Outline platelets.
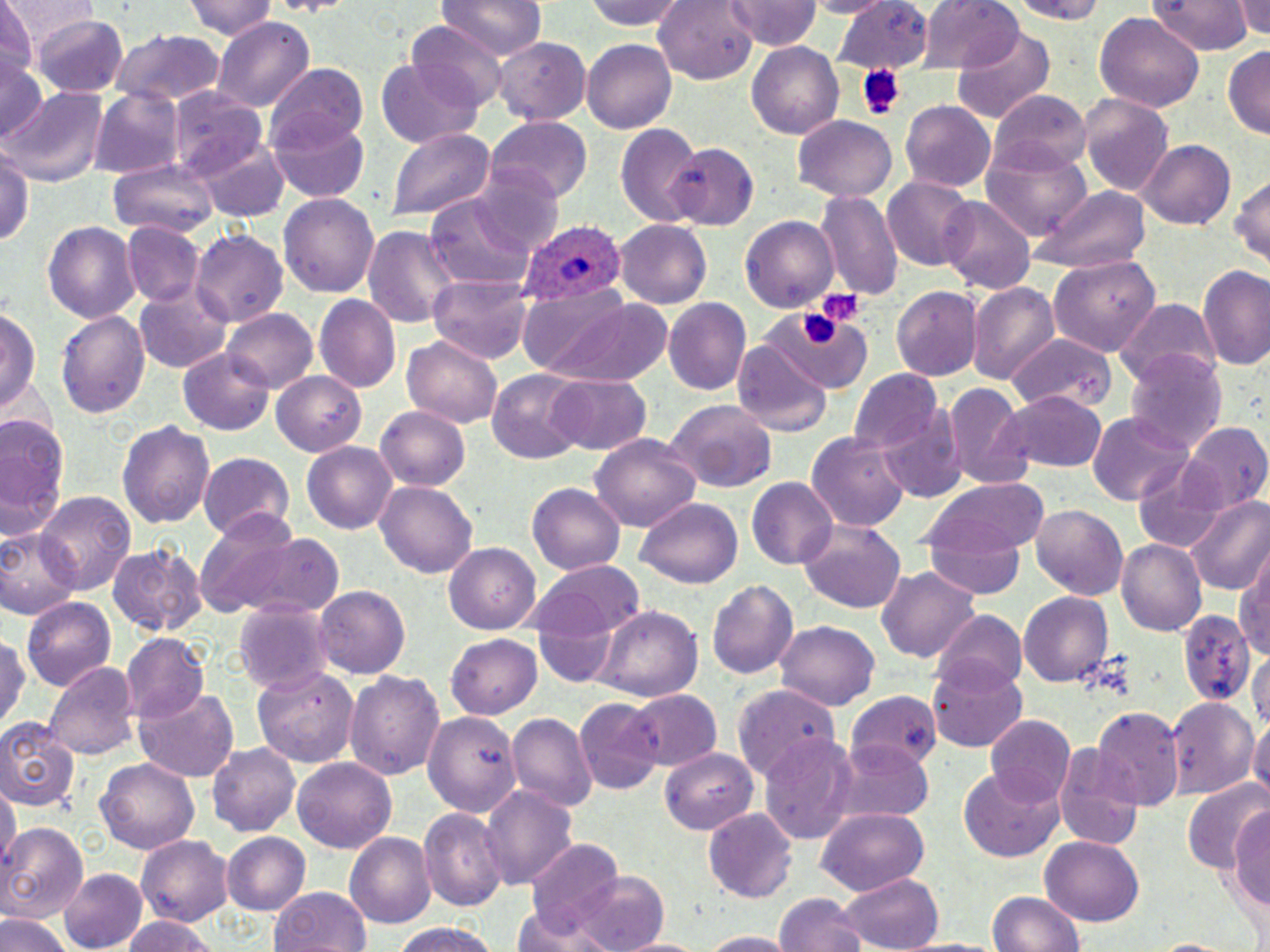

Approximate bounding boxes as [x1, y1, x2, y2] in pixels.
Platelets: [856, 63, 906, 121], [811, 288, 867, 327], [801, 312, 838, 344].

Summary:
  - Plasmodium ovale-infected red blood cell locations: [523, 222, 625, 304]
  - Uninfected red blood cell locations: [4, 0, 98, 54], [184, 0, 280, 39], [263, 0, 353, 17], [438, 0, 546, 63], [581, 0, 695, 33], [807, 0, 888, 17], [924, 0, 1023, 71], [1000, 0, 1117, 22], [1148, 0, 1255, 55], [1235, 0, 1270, 43], [653, 1, 756, 82], [835, 2, 933, 76], [725, 3, 824, 51], [0, 4, 38, 83], [1093, 11, 1205, 111], [33, 14, 130, 94], [213, 18, 313, 110], [406, 23, 509, 109], [952, 28, 1055, 122], [110, 30, 224, 107], [493, 38, 588, 124], [582, 39, 676, 134], [747, 41, 844, 139], [1223, 47, 1270, 140], [374, 58, 484, 146], [0, 60, 49, 141], [265, 64, 370, 150], [167, 85, 268, 181], [4, 88, 107, 188], [89, 90, 185, 179], [991, 91, 1092, 176], [1077, 94, 1173, 195], [901, 102, 997, 193], [483, 116, 592, 203], [792, 117, 897, 201], [270, 118, 371, 204], [614, 124, 702, 225], [386, 129, 493, 222], [1140, 139, 1233, 230], [202, 140, 289, 223], [0, 143, 35, 254], [666, 143, 756, 228], [982, 148, 1094, 241], [109, 160, 219, 238], [1231, 168, 1270, 271], [883, 177, 976, 271], [1028, 186, 1152, 272], [817, 189, 903, 300], [279, 192, 380, 300], [423, 193, 544, 290], [940, 197, 1034, 293], [741, 215, 840, 313], [616, 220, 714, 309], [43, 221, 139, 322], [123, 223, 207, 308], [363, 225, 462, 330], [191, 230, 288, 326], [1047, 255, 1162, 357], [1197, 264, 1270, 372], [429, 274, 535, 364], [968, 284, 1057, 384], [135, 286, 232, 373], [892, 288, 982, 379], [313, 295, 400, 394], [530, 295, 678, 387], [663, 298, 751, 396], [1114, 299, 1218, 392], [1, 303, 41, 422], [764, 306, 873, 391], [56, 308, 151, 420], [222, 308, 317, 389], [400, 332, 505, 428], [1007, 334, 1113, 415], [733, 344, 834, 437], [179, 347, 276, 436], [1125, 348, 1228, 455], [489, 369, 588, 462], [848, 369, 944, 453], [547, 373, 652, 455], [272, 374, 368, 455], [942, 382, 1033, 490], [1004, 388, 1106, 471], [665, 401, 777, 492], [375, 406, 472, 493], [880, 406, 968, 502], [0, 410, 68, 541], [1086, 410, 1196, 503], [117, 419, 214, 529], [1184, 423, 1269, 511], [806, 429, 911, 533], [592, 434, 701, 531], [302, 442, 401, 533], [197, 453, 294, 541], [1129, 454, 1234, 557], [376, 479, 479, 579], [747, 479, 836, 570], [925, 480, 1051, 560], [529, 482, 625, 574], [37, 490, 134, 595], [636, 497, 742, 588], [1187, 497, 1270, 595], [1030, 504, 1129, 600], [794, 517, 907, 615], [201, 522, 345, 621], [925, 522, 1029, 598], [1, 526, 79, 618], [108, 541, 207, 641], [1117, 541, 1206, 635], [444, 545, 540, 633], [1235, 553, 1270, 665], [534, 560, 644, 641], [877, 566, 979, 664], [707, 577, 799, 679], [313, 585, 410, 678], [1018, 591, 1115, 687], [22, 598, 116, 692], [233, 600, 332, 692], [1174, 604, 1254, 711], [594, 607, 703, 701], [931, 612, 1027, 697], [776, 620, 879, 712], [537, 625, 618, 686], [0, 626, 28, 732], [122, 634, 210, 722], [448, 634, 543, 718], [1251, 649, 1270, 737], [929, 656, 1029, 751], [44, 662, 139, 762], [252, 665, 358, 767], [346, 671, 445, 783], [733, 682, 842, 781], [135, 688, 240, 781], [623, 688, 722, 771], [849, 692, 942, 778], [1166, 696, 1259, 801], [574, 699, 662, 793], [423, 709, 520, 816], [1093, 709, 1183, 810], [506, 713, 595, 812], [1250, 714, 1270, 807], [984, 715, 1074, 801], [0, 716, 82, 808], [759, 735, 861, 843], [832, 739, 934, 824], [207, 742, 303, 835], [1054, 745, 1145, 850], [662, 749, 757, 834], [292, 758, 397, 854], [97, 760, 198, 852], [958, 769, 1067, 863], [1185, 778, 1268, 873], [1, 780, 18, 870], [483, 786, 578, 892], [1228, 805, 1270, 921], [703, 806, 798, 902], [420, 808, 506, 911], [815, 808, 931, 892], [1, 822, 88, 922], [220, 833, 309, 913], [343, 833, 435, 928], [136, 834, 232, 927], [1041, 835, 1145, 926], [525, 837, 626, 936], [61, 870, 146, 950], [576, 872, 670, 952], [839, 872, 945, 951], [269, 887, 372, 952], [985, 891, 1087, 952], [773, 894, 868, 952], [515, 910, 611, 952], [0, 914, 73, 952], [120, 916, 221, 952], [386, 922, 507, 952], [697, 929, 794, 950], [620, 933, 713, 952], [899, 936, 1005, 952]
  - Slide-level diagnosis: Plasmodium ovale
  - Image size: 1270×952 pixels
  - Magnification: 1000x
  - Stain: May-Grünwald-Giemsa
  - Preparation: thin blood smear
  - Modality: light microscopy
  - Field of view: single